Report the malaria status of this cell.
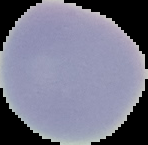
It is uninfected.

Summary:
  - Image size: 148×145 pixels
  - Image type: segmented cell region on a black background
  - Preparation: thin blood film